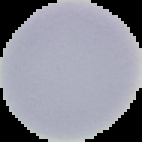 Image is 142×142 pixels. Segmented cell region on a black background. From a thin blood smear. Malaria status: uninfected.